Identify the blood parasite species.
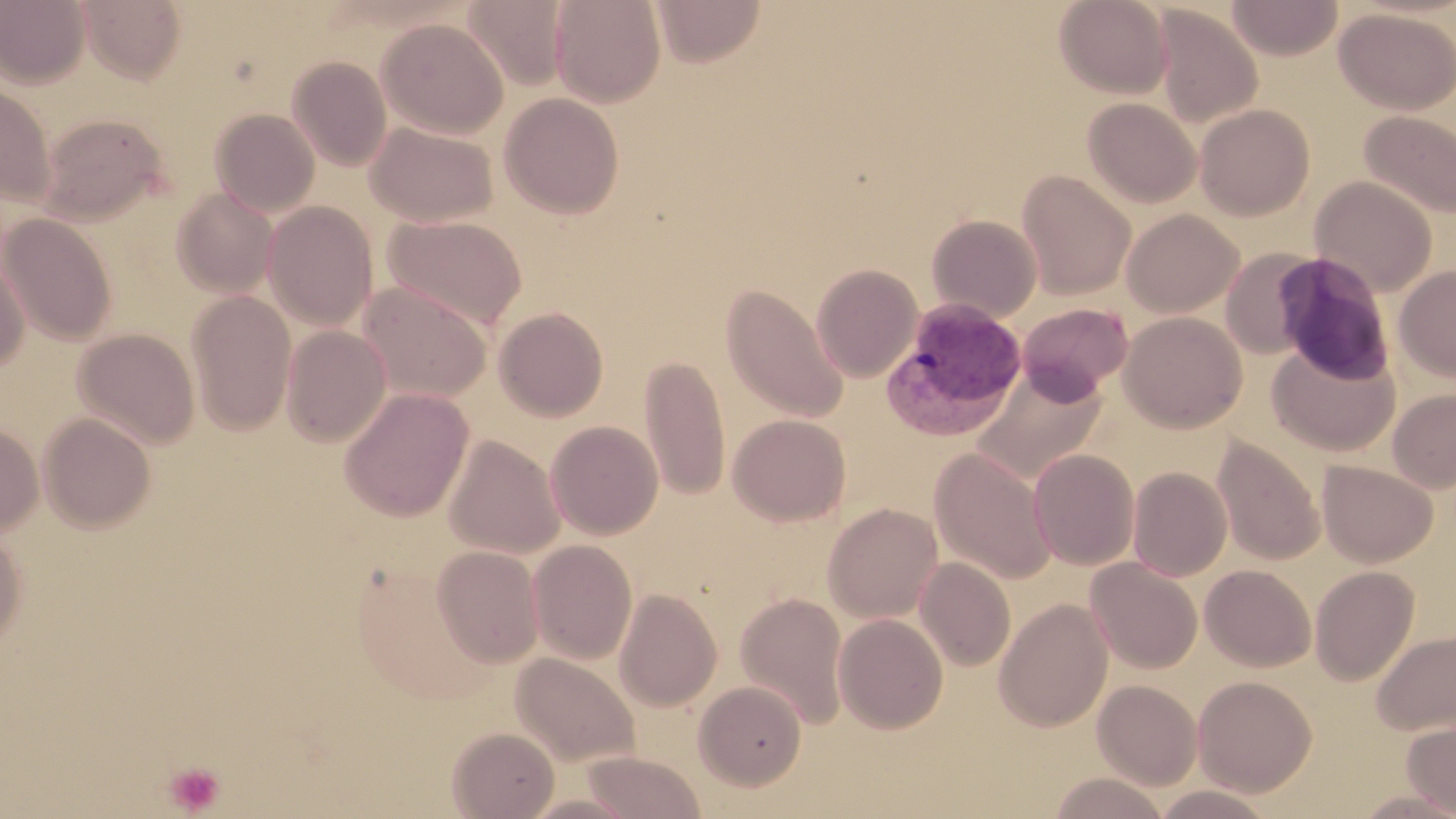
Plasmodium vivax.

{
  "stain": "May-Grünwald-Giemsa",
  "uninfected_red_blood_cell_locations": "approximate bounding boxes as (x1,y1)-(x2,y2) corner pairs in pixels: (77,0)-(187,84), (651,0)-(766,66), (1054,0)-(1173,99), (1226,0)-(1344,60), (0,1)-(92,89), (461,1)-(570,91), (550,1)-(666,107), (1152,6)-(1263,128), (1334,7)-(1456,114), (376,17)-(508,138), (287,56)-(392,171), (0,83)-(57,208), (499,92)-(624,219), (1082,97)-(1201,207), (1194,104)-(1315,220), (210,108)-(320,217), (1359,109)-(1456,220), (37,113)-(170,225), (365,121)-(499,227), (1017,171)-(1136,299), (1310,176)-(1437,296), (171,187)-(278,297), (263,201)-(378,330), (1121,209)-(1244,317), (1,213)-(117,345), (927,214)-(1043,322), (384,215)-(528,331), (1221,248)-(1322,359), (0,249)-(31,372), (811,263)-(923,382), (1394,265)-(1456,382), (358,281)-(493,402), (721,284)-(849,423), (186,291)-(296,435), (1017,303)-(1133,402), (493,307)-(609,421), (1119,311)-(1247,432), (280,325)-(392,447), (73,328)-(200,449), (1267,341)-(1399,456), (639,354)-(730,502), (973,368)-(1108,484), (339,387)-(474,522), (1388,388)-(1456,493), (38,412)-(156,533), (727,414)-(851,526), (545,421)-(664,540), (0,423)-(44,535), (443,435)-(565,559), (1212,436)-(1326,566), (929,447)-(1057,584), (1028,448)-(1140,570), (1317,459)-(1438,567), (1128,467)-(1232,581), (823,502)-(943,623), (0,528)-(27,652), (528,540)-(637,664), (431,545)-(544,667), (916,557)-(1015,671), (1086,558)-(1202,673), (1201,565)-(1316,672), (1309,566)-(1420,685), (614,588)-(723,711), (735,591)-(850,729), (994,598)-(1113,732), (833,613)-(948,733), (1372,630)-(1456,735), (511,653)-(640,767), (1193,675)-(1317,796), (1092,679)-(1202,790), (694,680)-(807,790), (1401,716)-(1456,815), (447,727)-(560,818), (580,751)-(707,818), (1047,772)-(1171,818), (1151,785)-(1277,819), (1350,788)-(1456,818)",
  "modality": "light microscopy",
  "preparation": "thin blood smear",
  "magnification": "1000x",
  "platelet_locations": "approximate bounding boxes as (x1,y1)-(x2,y2) corner pairs in pixels: (163,760)-(225,815)",
  "field_of_view": "single",
  "plasmodium_vivax_infected_red_blood_cell_locations": "approximate bounding boxes as (x1,y1)-(x2,y2) corner pairs in pixels: (880,297)-(1028,441)",
  "image_size": "1456×819 pixels"
}